Outline each blood parasite and name the species.
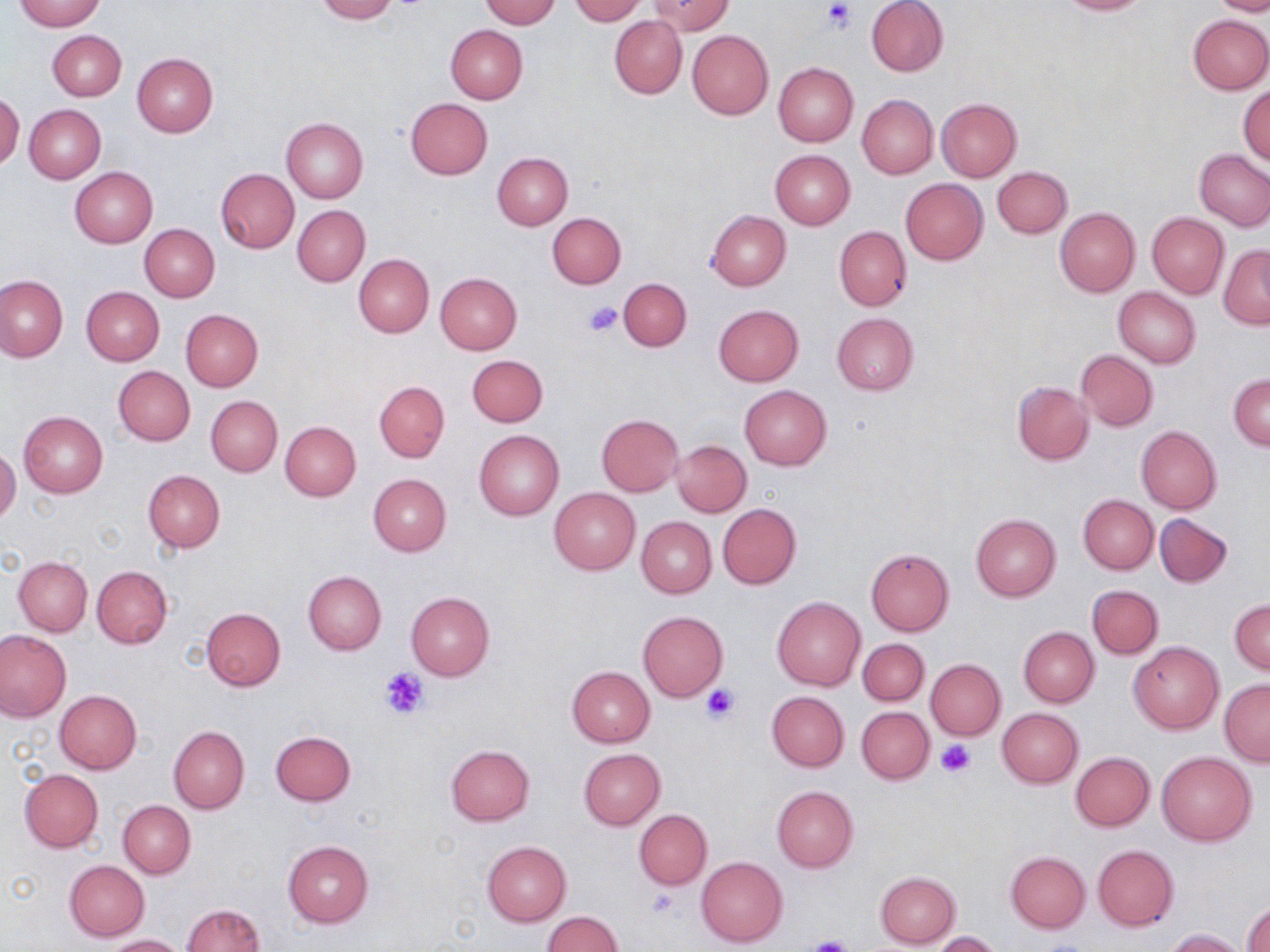
No blood parasites seen.

Summary:
  - Coordinate format: approximate bounding boxes as (x1, y1, x2, y2) in pixels
  - Uninfected red blood cell locations: (15, 0, 105, 31), (314, 0, 396, 23), (481, 0, 559, 27), (569, 0, 646, 24), (649, 0, 733, 35), (866, 0, 949, 77), (1053, 0, 1153, 15), (1210, 0, 1270, 16), (1187, 13, 1269, 94), (610, 16, 686, 98), (445, 24, 528, 103), (48, 30, 126, 100), (687, 30, 774, 120), (132, 53, 219, 136), (772, 62, 858, 147), (1239, 87, 1270, 165), (0, 93, 23, 170), (856, 94, 938, 179), (935, 97, 1022, 182), (405, 98, 492, 179), (24, 104, 106, 183), (281, 117, 368, 203), (770, 150, 855, 229), (1194, 150, 1270, 230), (492, 152, 573, 229), (993, 166, 1072, 238), (70, 167, 157, 247), (217, 169, 299, 253), (900, 178, 987, 265), (293, 205, 370, 286), (1055, 208, 1140, 297), (708, 210, 791, 290), (547, 212, 625, 287), (1147, 212, 1228, 298), (138, 223, 220, 302), (834, 226, 911, 311), (1218, 244, 1270, 329), (353, 254, 433, 338), (436, 273, 522, 355), (0, 274, 67, 362), (618, 277, 692, 350), (81, 287, 165, 366), (1113, 288, 1201, 368), (713, 304, 803, 386), (180, 309, 263, 390), (831, 313, 919, 394), (1076, 350, 1158, 430), (467, 355, 548, 427), (113, 366, 195, 446), (1229, 373, 1269, 451), (1012, 380, 1094, 464), (374, 381, 449, 462), (739, 385, 832, 470), (205, 395, 283, 477), (19, 411, 108, 498), (596, 414, 684, 495), (281, 421, 361, 501), (1136, 426, 1222, 514), (474, 431, 564, 519), (671, 440, 751, 516), (0, 447, 20, 524), (143, 469, 225, 553), (368, 473, 451, 556), (549, 487, 641, 575), (1077, 494, 1158, 574), (718, 504, 802, 590), (1154, 512, 1233, 588), (970, 513, 1061, 600), (637, 517, 717, 598), (865, 548, 954, 636), (13, 556, 92, 636), (92, 566, 171, 649), (303, 571, 387, 655), (1087, 585, 1163, 659), (406, 591, 494, 681), (772, 596, 866, 691), (1229, 598, 1270, 674), (202, 607, 286, 690), (638, 611, 728, 701), (1018, 626, 1099, 707), (0, 630, 71, 721), (858, 638, 928, 705), (1129, 642, 1223, 733), (926, 658, 1005, 740), (566, 665, 655, 747), (1219, 679, 1270, 766), (55, 690, 141, 775), (767, 691, 850, 771), (856, 706, 934, 785), (996, 708, 1083, 788), (169, 726, 249, 813), (270, 730, 356, 806), (446, 745, 535, 826), (579, 749, 665, 830), (1071, 752, 1154, 830), (1157, 752, 1256, 845), (20, 769, 103, 852), (771, 786, 858, 871), (118, 800, 194, 878), (634, 810, 711, 889), (283, 840, 373, 927), (482, 841, 571, 927), (1092, 844, 1180, 931), (1005, 850, 1091, 933), (696, 856, 789, 947), (64, 860, 149, 941), (875, 872, 961, 948), (1244, 903, 1269, 952), (183, 904, 265, 952), (542, 912, 623, 952), (1166, 929, 1248, 952), (932, 931, 1003, 951), (103, 934, 188, 952)
  - Platelet locations: (820, 2, 858, 33), (584, 301, 624, 337), (381, 667, 430, 718), (701, 684, 742, 723), (938, 740, 977, 777), (646, 889, 680, 919), (800, 937, 858, 952)
  - Slide-level diagnosis: no evidence of blood parasites
  - Field of view: single
  - Stain: May-Grünwald-Giemsa
  - Image size: 1270×952 pixels
  - Preparation: thin blood smear
  - Magnification: 1000x
  - Modality: light microscopy